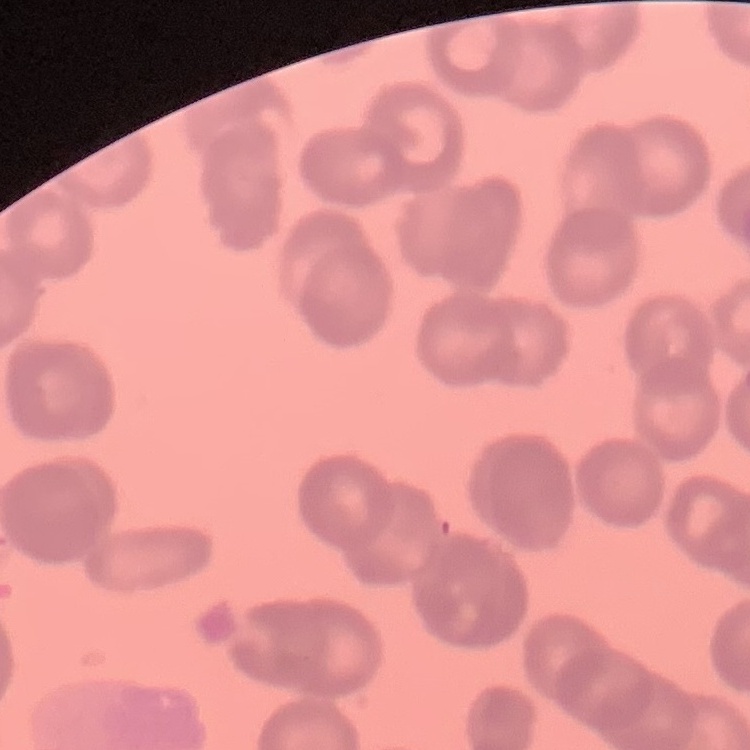 The erythrocytes exhibit rouleaux formation. Square crop of a larger photomicrograph. Stained with either Field's or Giemsa. Thin blood smear.